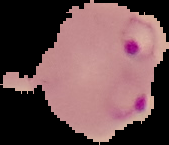

result = Plasmodium parasites detected
image size = 169×145 pixels
image type = segmented cell region on a black background
preparation = thin blood film